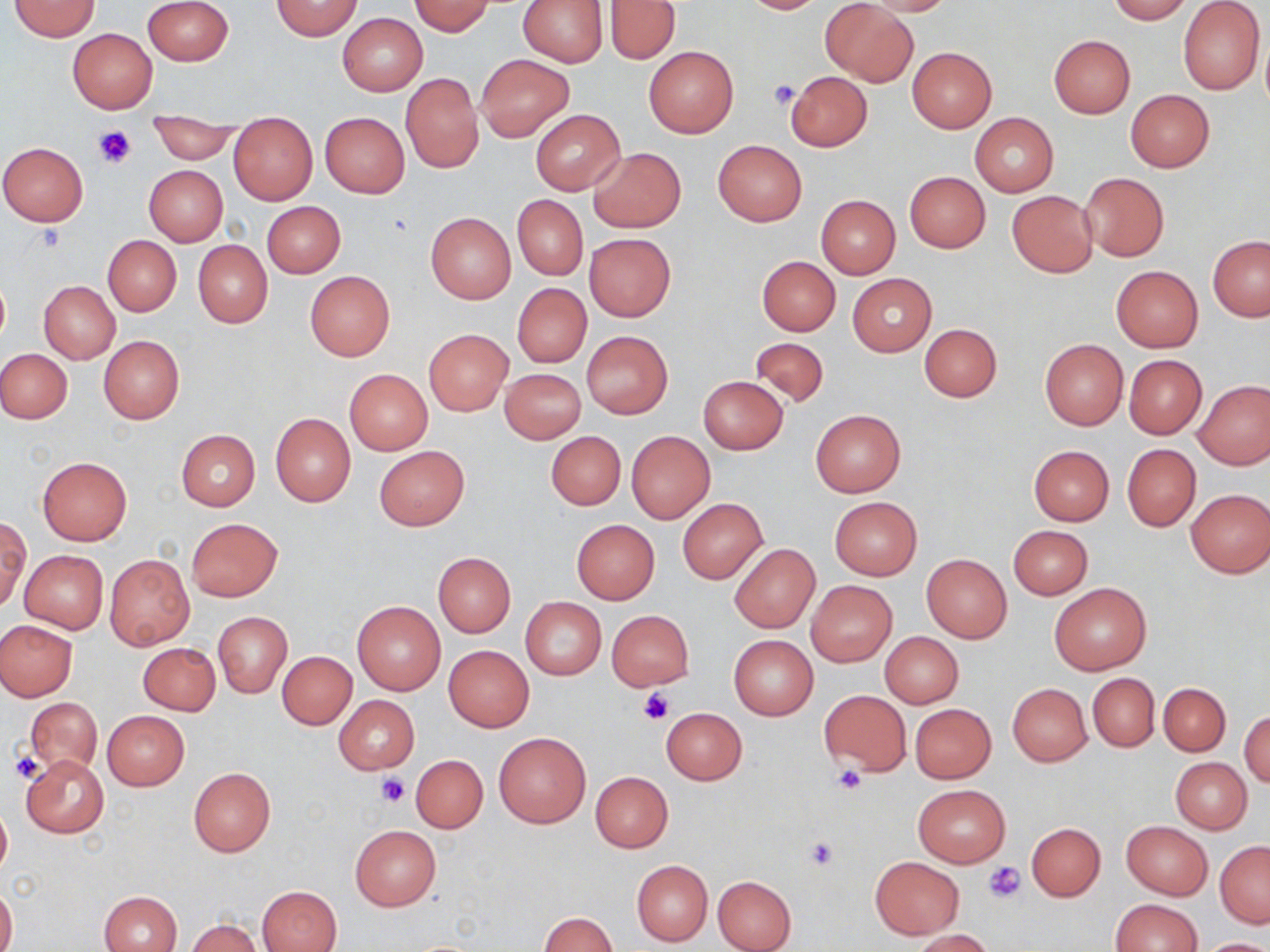

Summary:
  - Coordinate format: approximate bounding boxes as (x1, y1, x2, y2) in pixels
  - Uninfected red blood cell locations: (142, 0, 233, 66), (517, 0, 608, 67), (738, 0, 830, 14), (857, 0, 959, 16), (1106, 0, 1190, 23), (1178, 0, 1266, 95), (9, 1, 101, 40), (273, 1, 361, 40), (409, 1, 496, 36), (820, 1, 918, 87), (605, 2, 680, 64), (337, 13, 427, 95), (67, 28, 157, 113), (1049, 34, 1136, 118), (644, 46, 738, 137), (907, 48, 997, 133), (476, 54, 573, 140), (785, 71, 872, 152), (401, 73, 483, 173), (1126, 90, 1215, 172), (530, 109, 625, 195), (148, 111, 239, 164), (320, 112, 410, 197), (969, 112, 1059, 196), (229, 113, 317, 204), (713, 140, 806, 226), (0, 143, 88, 226), (590, 148, 685, 232), (144, 165, 228, 245), (905, 171, 990, 253), (1078, 172, 1169, 261), (1006, 190, 1098, 278), (512, 195, 587, 280), (816, 195, 900, 278), (262, 201, 345, 278), (426, 213, 516, 303), (584, 233, 676, 321), (103, 235, 181, 316), (1208, 236, 1270, 321), (193, 241, 272, 327), (756, 255, 840, 335), (1111, 265, 1203, 353), (305, 271, 394, 359), (847, 273, 936, 356), (39, 281, 120, 363), (511, 283, 591, 368), (919, 323, 1002, 402), (424, 329, 513, 415), (582, 332, 673, 419), (99, 336, 185, 423), (750, 337, 830, 407), (1039, 339, 1128, 430), (1, 348, 72, 424), (1125, 355, 1206, 439), (499, 368, 585, 443), (344, 369, 432, 455), (698, 376, 788, 453), (1194, 378, 1270, 469), (811, 409, 906, 498), (271, 413, 356, 508), (176, 430, 260, 510), (545, 432, 626, 510), (625, 432, 714, 524), (1122, 444, 1201, 531), (374, 445, 470, 531), (1028, 445, 1115, 525), (37, 456, 132, 546), (1185, 489, 1269, 578), (830, 497, 922, 579), (677, 498, 767, 583), (1, 517, 30, 610), (186, 518, 283, 601), (571, 519, 660, 604), (1008, 525, 1092, 599), (729, 543, 820, 633), (20, 550, 107, 634), (431, 552, 516, 637), (105, 554, 195, 651), (921, 554, 1012, 642), (806, 581, 897, 666), (1049, 582, 1151, 675), (520, 598, 606, 678), (353, 600, 445, 695), (606, 610, 694, 691), (214, 612, 291, 698), (0, 619, 78, 700), (880, 631, 964, 709), (728, 634, 818, 720), (138, 643, 220, 715), (443, 645, 534, 731), (277, 651, 356, 729), (1087, 673, 1159, 752), (1158, 683, 1230, 756), (1007, 684, 1092, 766), (819, 689, 911, 776), (335, 696, 419, 773), (25, 697, 103, 777), (910, 704, 996, 783), (661, 707, 746, 785), (1240, 710, 1269, 788), (102, 711, 189, 790), (494, 732, 590, 829), (22, 755, 108, 837), (411, 755, 487, 832), (1170, 757, 1252, 834), (189, 767, 276, 855), (591, 772, 673, 852), (913, 784, 1011, 867), (0, 800, 11, 880), (1121, 820, 1213, 900), (1026, 822, 1106, 900), (350, 824, 442, 910), (1215, 841, 1270, 927), (870, 856, 964, 938), (631, 860, 713, 946), (713, 875, 795, 951), (1, 883, 16, 952), (258, 885, 342, 952), (100, 890, 183, 952), (1109, 899, 1201, 952), (538, 912, 617, 952), (186, 918, 263, 952), (911, 930, 996, 951), (1198, 938, 1270, 952)
  - Platelet locations: (768, 79, 798, 109), (94, 126, 137, 169), (638, 690, 673, 726), (8, 751, 45, 783), (834, 766, 867, 795), (376, 773, 410, 806), (804, 836, 839, 870), (985, 861, 1025, 903)
  - Slide-level diagnosis: no evidence of blood parasites
  - Image size: 1270×952 pixels
  - Stain: May-Grünwald-Giemsa
  - Modality: light microscopy
  - Magnification: 1000x
  - Field of view: one of a larger specimen
  - Preparation: thin blood smear